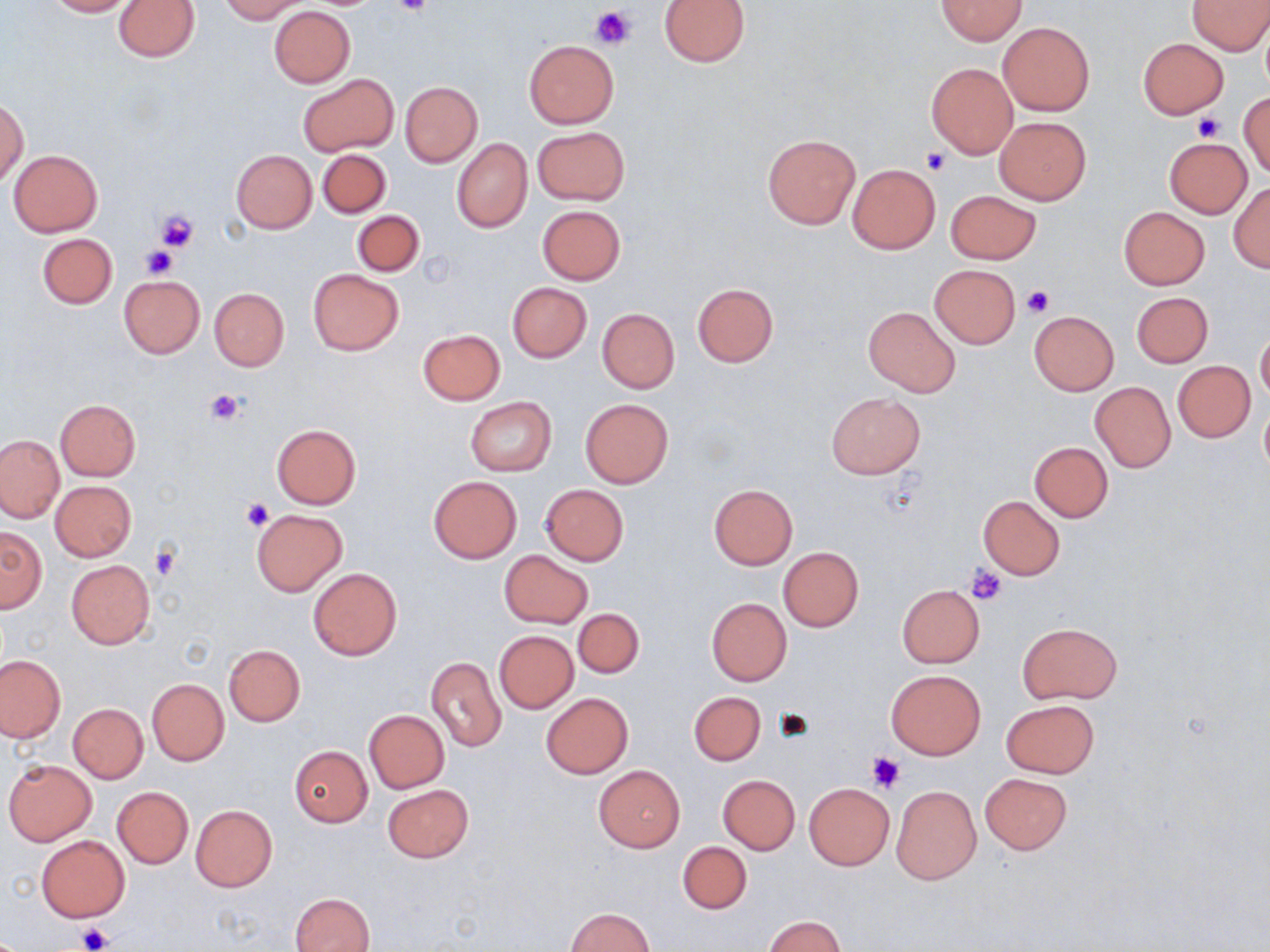

Approximate bounding boxes as (x1,y1)-(x2,y2) corner pairs in pixels. Platelet locations: (393,0)-(434,17), (590,5)-(635,50), (1193,112)-(1225,143), (921,147)-(952,175), (154,209)-(198,252), (140,247)-(176,278), (1021,285)-(1053,318), (206,389)-(244,426), (241,498)-(274,533), (150,544)-(182,581), (965,564)-(1008,605), (772,708)-(815,743), (866,751)-(906,792), (76,924)-(112,950). Uninfected red blood cell locations: (45,0)-(135,17), (218,0)-(308,22), (936,0)-(1027,44), (1189,0)-(1270,54), (114,1)-(197,61), (658,1)-(750,66), (269,7)-(355,86), (998,20)-(1095,116), (1260,21)-(1270,95), (1137,37)-(1228,118), (523,39)-(619,128), (926,63)-(1017,158), (298,75)-(396,156), (399,81)-(483,167), (1239,91)-(1270,180), (1,99)-(28,186), (995,117)-(1091,204), (532,126)-(629,204), (762,134)-(861,230), (1165,136)-(1253,216), (452,138)-(532,232), (9,149)-(103,236), (317,149)-(391,218), (232,150)-(317,232), (847,164)-(940,253), (1228,182)-(1270,273), (945,190)-(1041,264), (537,204)-(626,284), (1118,206)-(1209,290), (352,210)-(424,277), (38,233)-(117,309), (929,264)-(1021,348), (307,268)-(403,355), (118,275)-(204,357), (507,282)-(591,362), (692,283)-(778,367), (210,288)-(289,371), (1132,292)-(1213,368), (863,307)-(960,396), (598,308)-(679,393), (1029,311)-(1119,395), (1257,328)-(1270,405), (418,329)-(505,405), (1172,362)-(1255,442), (1089,381)-(1176,472), (826,392)-(925,480), (465,398)-(555,476), (55,399)-(142,481), (580,399)-(674,489), (1260,400)-(1270,475), (271,424)-(362,509), (0,435)-(65,523), (1028,441)-(1113,521), (429,476)-(522,562), (51,481)-(136,561), (540,484)-(629,565), (707,484)-(796,569), (978,497)-(1065,579), (252,509)-(347,595), (0,526)-(46,613), (778,547)-(863,631), (499,550)-(593,629), (66,559)-(155,648), (308,567)-(402,661), (896,584)-(984,668), (706,597)-(792,685), (572,608)-(643,679), (1018,621)-(1122,704), (494,630)-(579,713), (224,644)-(306,726), (425,655)-(506,753), (0,656)-(64,741), (886,669)-(985,759), (146,679)-(229,766), (689,691)-(765,765), (541,692)-(632,778), (1001,698)-(1100,779), (68,703)-(148,783), (363,709)-(449,792), (288,745)-(372,827), (3,759)-(97,846), (593,766)-(685,851), (980,772)-(1073,854), (718,775)-(800,854), (804,783)-(895,869), (383,784)-(473,863), (891,785)-(982,884), (112,786)-(193,869), (190,804)-(277,892), (36,836)-(130,922), (677,841)-(752,915), (291,891)-(375,952), (565,908)-(654,952), (762,915)-(847,951). Slide-level diagnosis: no evidence of blood parasites. Optical microscopy. Thin blood film. Image is 1270×952 pixels. Captured at 1000x magnification. One field of a larger specimen. May-Grünwald-Giemsa-stained preparation.